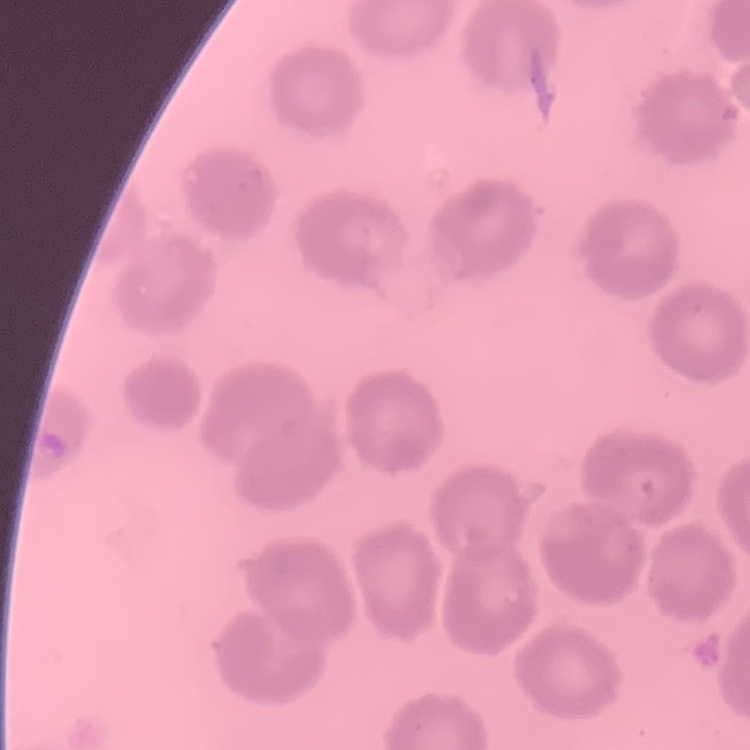
erythrocyte morphology = no rouleaux formation
image type = square crop of a larger photomicrograph
stain = Field's or Giemsa
preparation = thin blood film